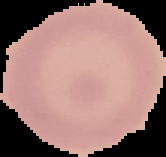
malaria status = uninfected
preparation = thin blood smear
image size = 166×157 pixels
image type = segmented cell region with the area outside set to black